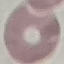

malaria status = uninfected
image type = cell patch, automatically extracted from a larger field of view and resized to 64 × 64 pixels
capture = smartphone through the microscope eyepiece
stain = Giemsa
preparation = thin smear